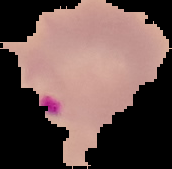 The area outside the segmented cell region is set to black. Image is 172×169 pixels. Malaria status: parasitized. From a thin blood smear.